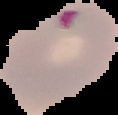
Image is 118×115 pixels. From a thin blood film. Malaria status: parasitized. Cell region segmented out of the field of view; the surrounding area is masked to black.